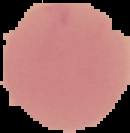
Summary:
  - Image type: segmented cell region with the area outside set to black
  - Image size: 130×133 pixels
  - Preparation: thin blood smear
  - Malaria status: uninfected